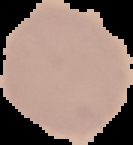

preparation = thin blood smear
result = no malaria parasites seen
image size = 133×145 pixels
image type = segmented cell region on a black background